Give the extent of all uninfected red blood cells.
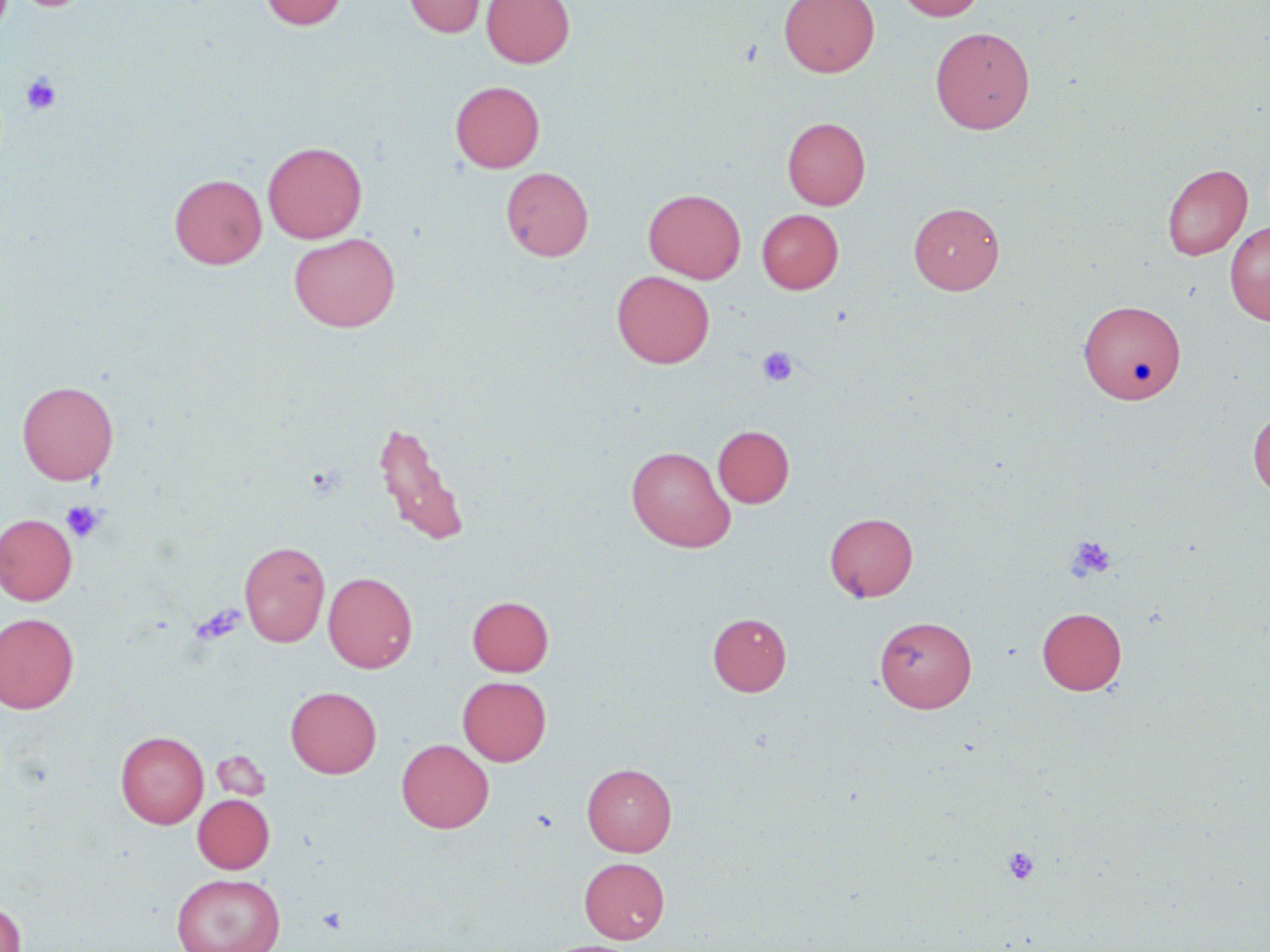
Approximate bounding boxes as (x1,y1)-(x2,y2) corner pairs in pixels.
Uninfected red blood cells: (9,0)-(95,13), (260,0)-(348,30), (405,0)-(485,37), (481,0)-(575,67), (779,0)-(879,77), (897,0)-(986,21), (930,27)-(1035,134), (450,80)-(545,173), (783,117)-(870,210), (263,141)-(367,243), (1162,163)-(1252,260), (501,167)-(593,261), (169,174)-(266,269), (644,189)-(746,282), (909,202)-(1004,294), (757,209)-(843,294), (1225,221)-(1270,325), (290,233)-(400,332), (612,271)-(715,368), (1079,299)-(1185,404), (17,380)-(119,484), (1248,410)-(1270,498), (374,420)-(470,547), (713,425)-(794,508), (626,446)-(736,552), (825,512)-(917,601), (0,514)-(77,605), (239,541)-(329,647), (323,571)-(417,673), (467,596)-(553,676), (1037,607)-(1126,695), (708,612)-(791,696), (0,613)-(79,713), (875,616)-(976,712), (458,676)-(551,766), (286,686)-(381,778), (116,731)-(208,828), (396,738)-(493,833), (212,750)-(270,802), (582,763)-(677,856), (193,794)-(274,873), (579,857)-(669,944), (171,872)-(285,952), (0,902)-(27,952), (536,940)-(640,952).

slide-level diagnosis = negative for blood parasites
modality = light microscopy
field of view = single
stain = May-Grünwald-Giemsa
image size = 1270×952 pixels
preparation = thin blood smear
platelet locations = approximate bounding boxes as (x1,y1)-(x2,y2) corner pairs in pixels: (21,74)-(62,116), (757,346)-(798,386), (61,501)-(105,542), (1066,535)-(1117,581), (189,604)-(246,646), (1002,846)-(1040,885), (317,907)-(348,933)
magnification = 1000x